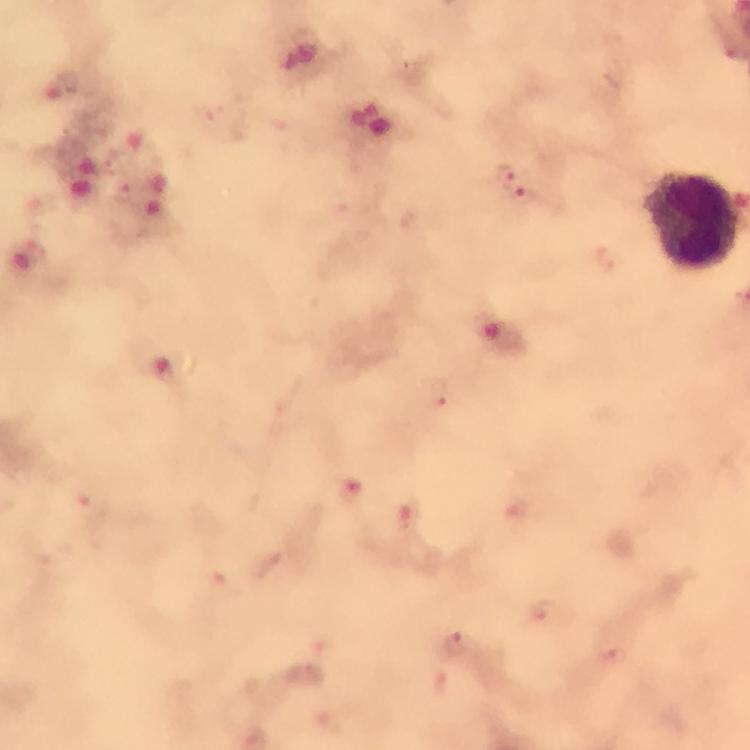

capture: smartphone camera through the microscope
preparation: thick smear
immersion_oil: used
image_size: 750×750 pixels
plasmodium_parasite_locations: 'approximate centers as {x, y} in pixels: {505, 173}, {123, 192}, {524, 195}, {439, 393}, {350, 491}, {91, 510}, {408, 519}, {271, 567}, {542, 612}, {456, 645}, {610, 655}'
cropped_from: a single field of view
magnification: 100x
leukocyte_locations: 'approximate centers as {x, y} in pixels: {695, 220}'
context: from a diagnostic examination for malaria
stain: Giemsa